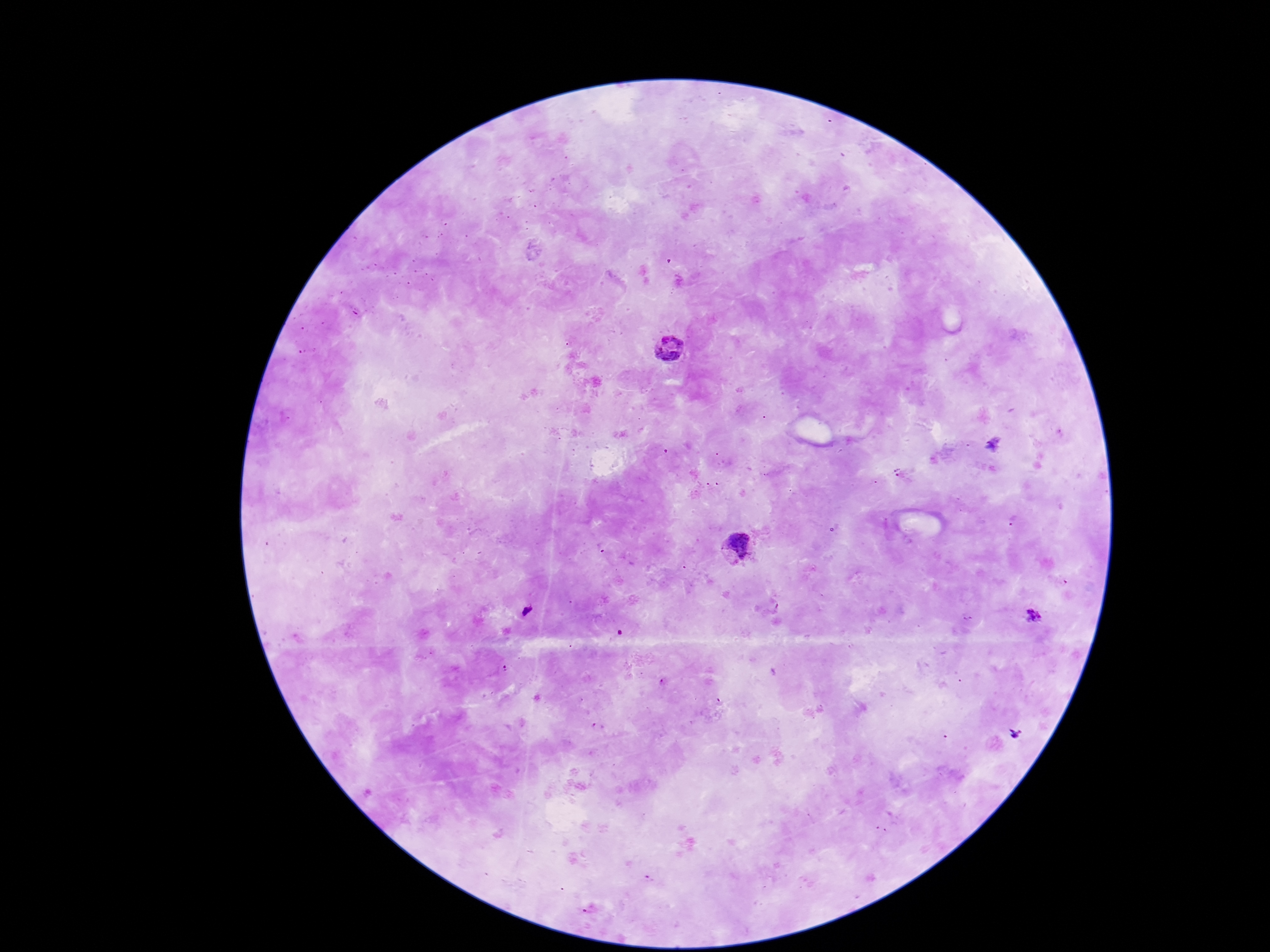
Approximate object centers, in pixels from the top-left corner. Plasmodium parasite locations: (x=667, y=349), (x=741, y=547), (x=527, y=610), (x=1032, y=616). One field from this slide. Photographed through the microscope eyepiece with a smartphone camera. Thick blood smear. Patient malaria status: infected. Giemsa-stained preparation. Image is 1270×952 pixels. 100x magnification.